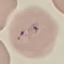
{
  "malaria_status": "uninfected",
  "stain": "Giemsa",
  "preparation": "thin blood film",
  "image_type": "automatically extracted cell patch, resized to 64 × 64 pixels",
  "capture": "smartphone camera at the microscope eyepiece"
}